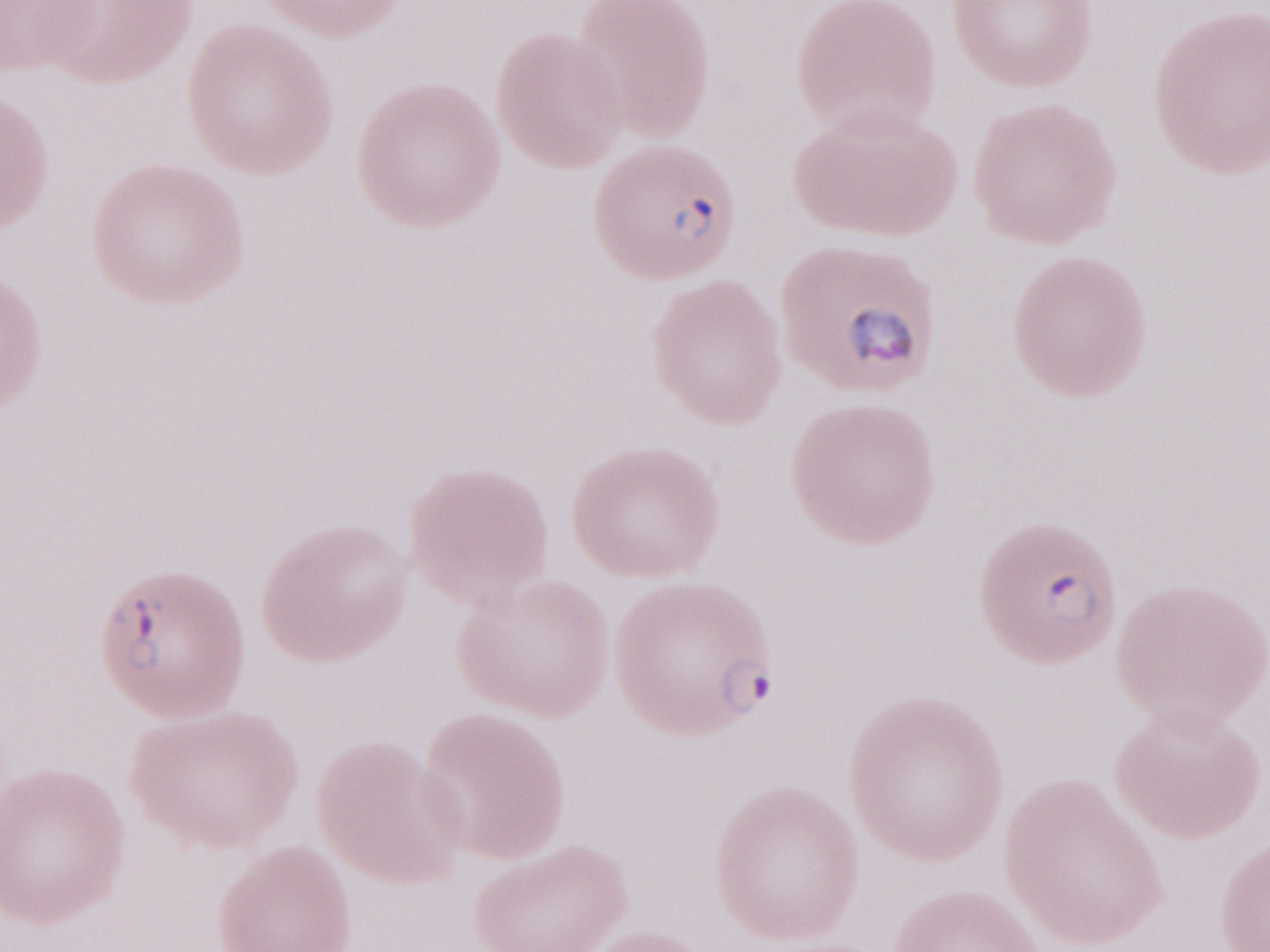

Malaria diagnosis (patient-level): positive. May-Grünwald-Giemsa stain. Single field of view. Thin peripheral-blood smear. 1,000x magnification. Olympus BX43 microscope, Olympus DP73 camera. Image is 1270×952 pixels.